Assess for malaria.
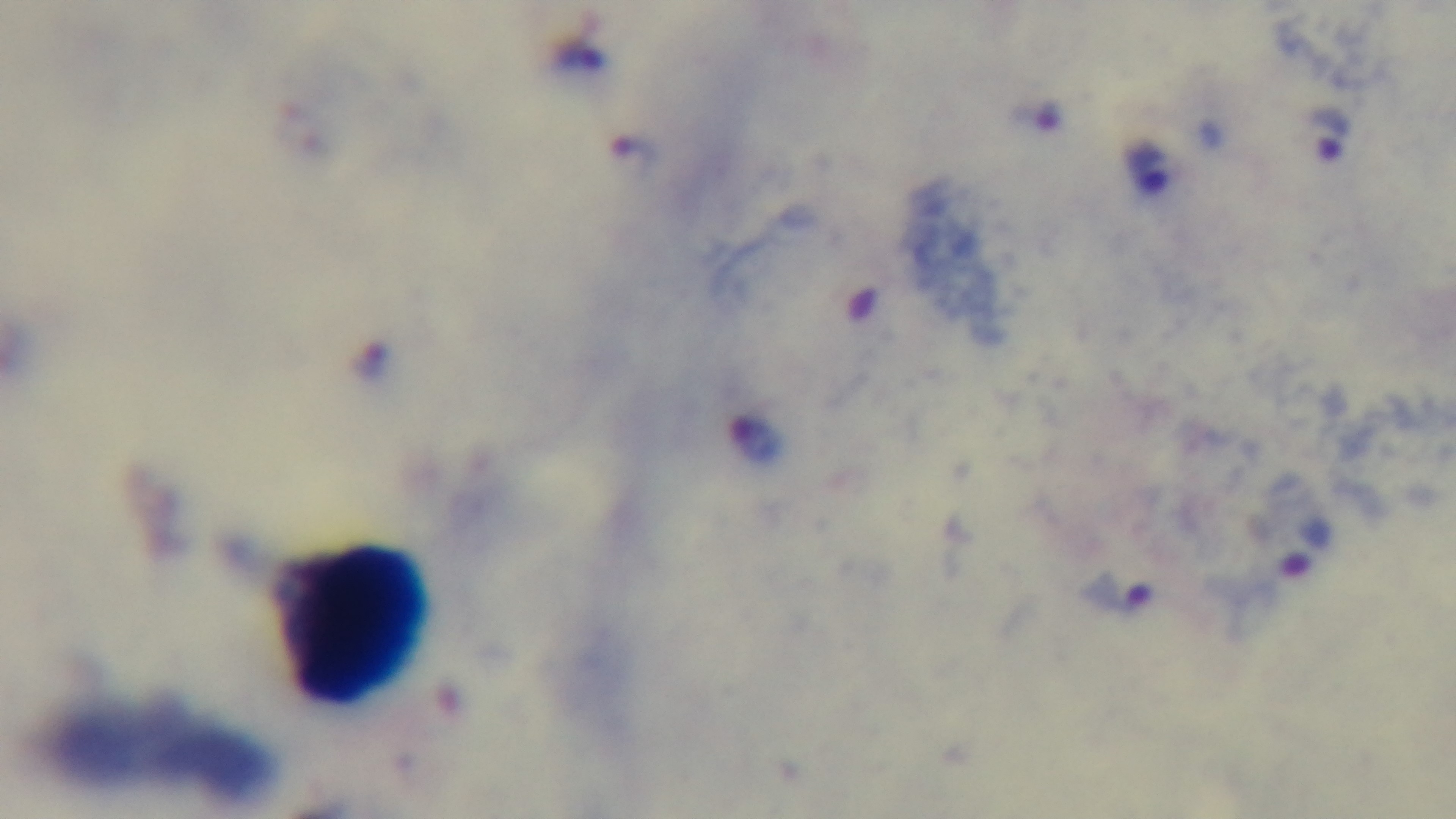
Infected.

Mounted 4K digital camera. One field from the slide. 100x oil-immersion objective. Light microscopy. Preparation: thick smear. Giemsa stain.